Describe the morphology of the red blood cells.
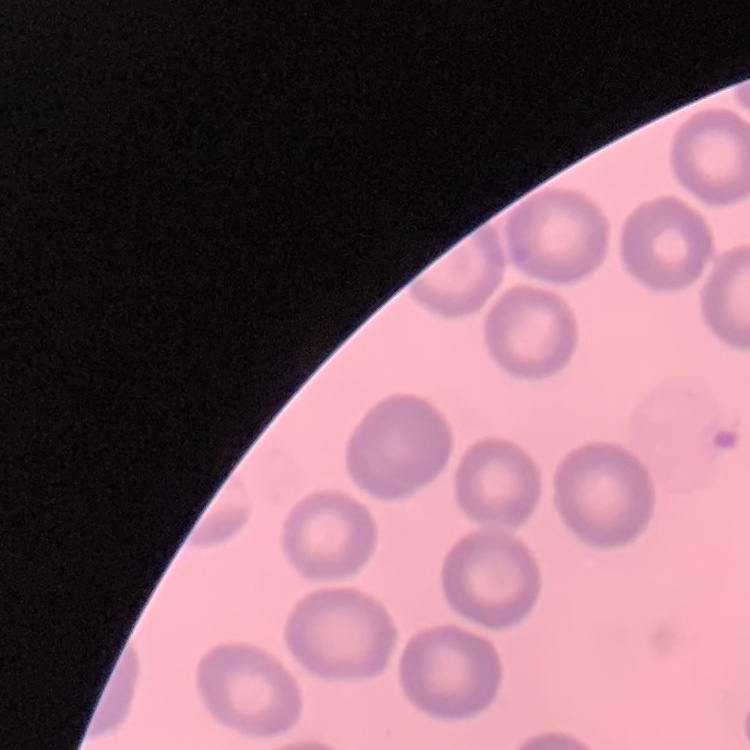

They show no rouleaux formation.

Summary:
  - Image type: square crop of a larger photomicrograph
  - Preparation: thin blood smear
  - Stain: Field's or Giemsa